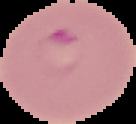

image type = segmented cell region on a black background
result = malaria parasites identified
preparation = thin blood smear
image size = 136×124 pixels